Outline each Plasmodium vivax-infected red blood cell.
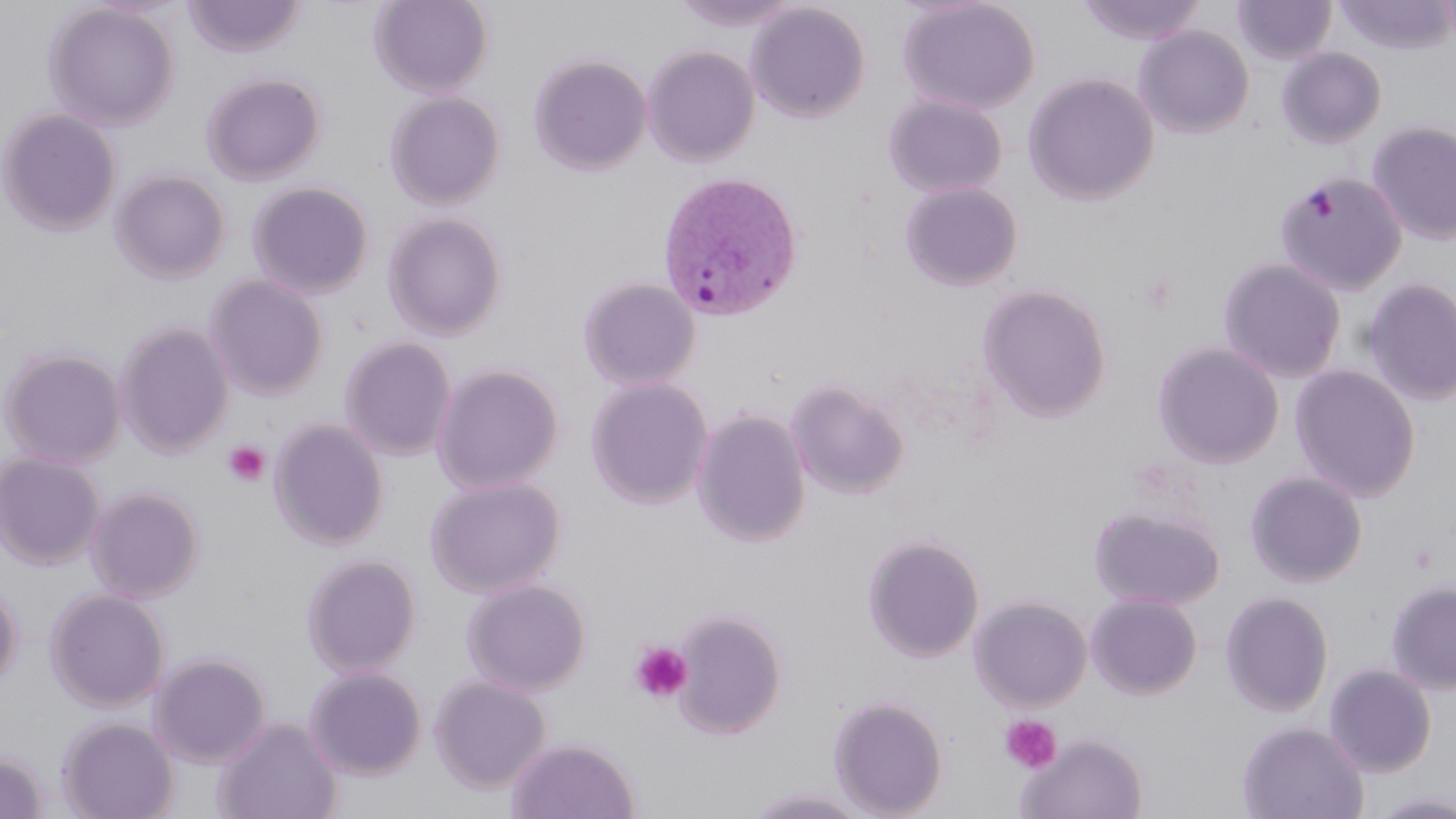

Approximate bounding boxes as (x1, y1, x2, y2) in pixels.
Plasmodium vivax-infected red blood cells: (656, 170, 804, 323).

Uninfected red blood cell locations: (369, 0, 493, 98), (672, 0, 802, 31), (897, 0, 1041, 115), (1075, 0, 1207, 45), (1232, 0, 1336, 65), (1334, 0, 1456, 54), (1436, 0, 1456, 48), (181, 1, 307, 59), (43, 2, 180, 132), (746, 3, 870, 123), (1133, 25, 1254, 139), (642, 45, 760, 167), (1276, 47, 1386, 148), (529, 54, 652, 175), (201, 72, 326, 185), (1022, 73, 1159, 206), (385, 91, 505, 209), (883, 93, 1008, 199), (0, 107, 121, 237), (1367, 121, 1456, 245), (110, 169, 230, 284), (1274, 172, 1408, 296), (247, 181, 373, 299), (899, 181, 1024, 291), (383, 212, 507, 340), (1217, 258, 1347, 382), (205, 274, 328, 400), (578, 276, 702, 392), (1361, 277, 1456, 406), (977, 283, 1112, 423), (114, 320, 235, 458), (338, 336, 457, 461), (1152, 341, 1285, 469), (0, 346, 128, 468), (432, 364, 564, 494), (1289, 364, 1421, 502), (585, 377, 714, 509), (786, 379, 910, 500), (691, 408, 812, 548), (269, 418, 388, 551), (0, 451, 106, 570), (1245, 470, 1368, 588), (425, 475, 565, 598), (86, 485, 205, 603), (1089, 504, 1226, 610), (862, 533, 985, 663), (301, 553, 421, 678), (461, 577, 591, 696), (1385, 579, 1456, 695), (0, 581, 23, 691), (45, 588, 170, 712), (1220, 590, 1334, 717), (1086, 592, 1203, 699), (969, 595, 1093, 711), (672, 609, 787, 739), (149, 652, 271, 768), (1324, 663, 1437, 777), (304, 665, 427, 780), (429, 675, 552, 794), (827, 695, 949, 818), (213, 715, 343, 819), (57, 716, 179, 819), (1237, 721, 1368, 819), (1016, 733, 1149, 819), (506, 737, 641, 819), (0, 751, 49, 818), (742, 786, 877, 818), (1362, 790, 1456, 819). Platelet locations: (1135, 271, 1181, 315), (222, 441, 270, 487), (629, 640, 693, 705), (999, 715, 1062, 774). Slide-level diagnosis: Plasmodium vivax. 1000x magnification. Thin blood smear. One field of a larger specimen. Image is 1456×819 pixels. May-Grünwald-Giemsa-stained preparation. Light microscopy.